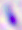
identification = Toxoplasma gondii
magnification = 400x
modality = photomicrograph